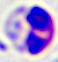
identification: leukocyte
magnification: 400x
modality: photomicrograph